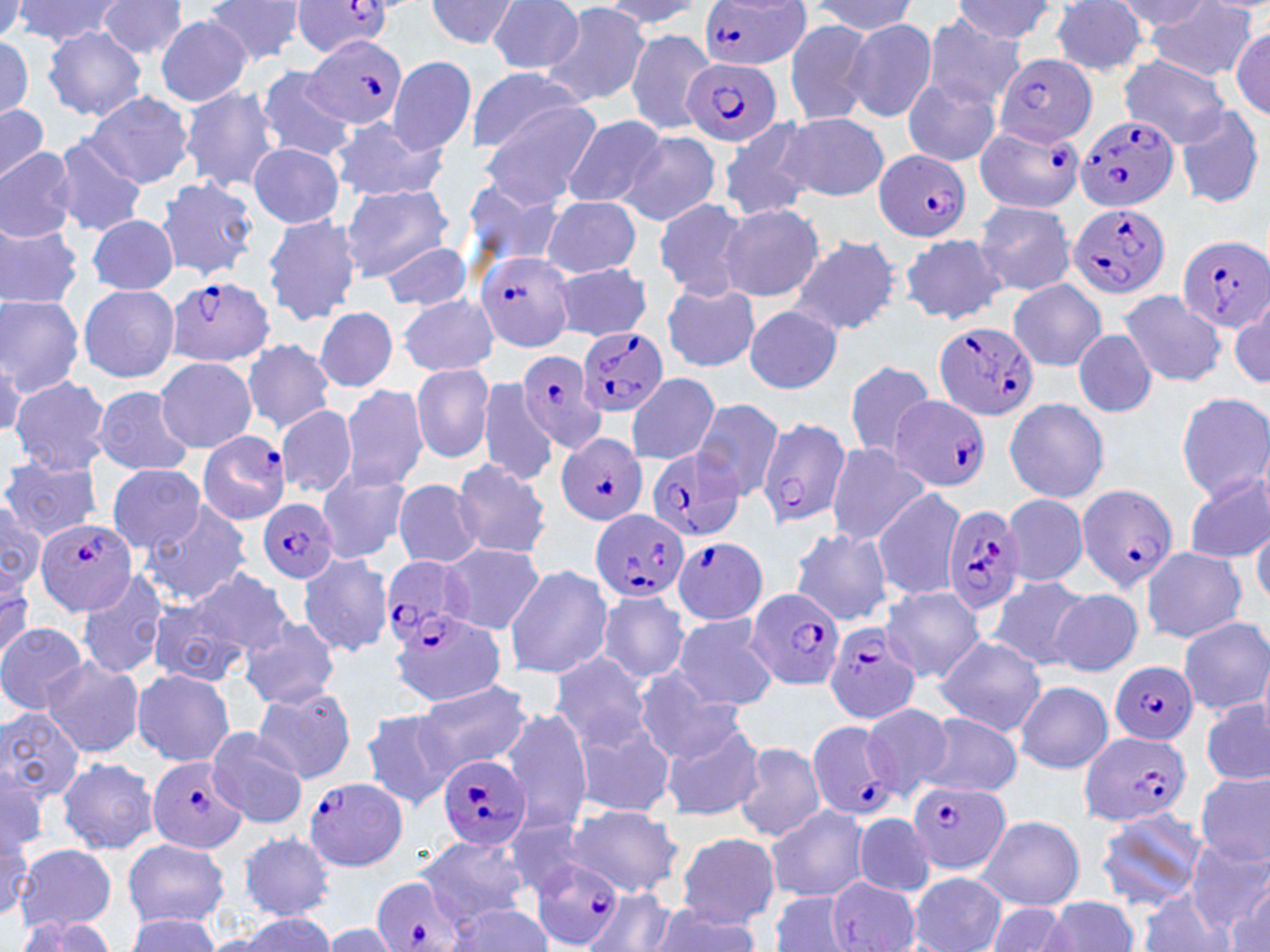
Summary:
  - Coordinate format: approximate bounding boxes as (x1, y1, x2, y2) in pixels
  - Uninfected red blood cell locations: (0, 0, 28, 38), (14, 0, 125, 47), (200, 0, 308, 65), (424, 0, 520, 51), (594, 0, 705, 29), (96, 1, 188, 60), (808, 1, 918, 35), (953, 1, 1058, 45), (1114, 1, 1216, 30), (486, 2, 585, 74), (538, 2, 653, 109), (1049, 2, 1152, 78), (1145, 2, 1257, 82), (155, 14, 255, 106), (781, 17, 879, 127), (923, 17, 1023, 111), (844, 19, 938, 122), (42, 25, 148, 121), (626, 27, 717, 135), (1231, 27, 1268, 118), (0, 31, 38, 121), (386, 56, 477, 156), (1118, 56, 1232, 147), (255, 65, 356, 162), (465, 68, 591, 154), (902, 77, 1001, 169), (178, 86, 282, 194), (84, 90, 195, 189), (478, 98, 605, 204), (0, 102, 52, 186), (1174, 105, 1266, 210), (779, 113, 888, 202), (564, 115, 668, 209), (717, 116, 817, 221), (328, 117, 447, 204), (548, 124, 656, 270), (619, 130, 722, 227), (51, 136, 149, 237), (247, 141, 345, 228), (0, 145, 77, 243), (456, 174, 567, 273), (155, 178, 259, 281), (339, 182, 457, 281), (541, 196, 642, 277), (653, 196, 750, 299), (974, 200, 1076, 296), (719, 203, 825, 301), (261, 212, 360, 328), (86, 214, 179, 295), (739, 214, 883, 320), (0, 221, 84, 310), (899, 231, 1008, 325), (788, 234, 900, 337), (376, 240, 473, 310), (550, 263, 652, 341), (1007, 279, 1107, 372), (661, 282, 760, 373), (78, 283, 181, 385), (1118, 290, 1227, 388), (0, 293, 86, 395), (398, 293, 498, 378), (1231, 294, 1269, 385), (742, 306, 845, 392), (312, 307, 399, 392), (1070, 329, 1159, 418), (244, 339, 337, 432), (0, 341, 27, 441), (155, 358, 258, 452), (843, 360, 938, 460), (411, 363, 496, 465), (625, 373, 721, 465), (9, 375, 111, 477), (477, 378, 560, 490), (339, 382, 429, 491), (91, 386, 195, 476), (1175, 391, 1270, 501), (1002, 398, 1111, 503), (692, 399, 787, 501), (276, 404, 358, 498), (825, 443, 930, 547), (2, 456, 104, 540), (451, 458, 550, 559), (105, 464, 206, 553), (314, 468, 415, 564), (1183, 471, 1269, 565), (393, 479, 482, 568), (871, 489, 968, 599), (1001, 492, 1089, 586), (139, 498, 254, 606), (0, 502, 47, 593), (1252, 514, 1269, 607), (789, 527, 894, 627), (440, 544, 543, 634), (1140, 546, 1246, 643), (296, 552, 394, 658), (0, 562, 38, 661), (504, 564, 612, 679), (187, 566, 295, 660), (74, 570, 171, 680), (986, 575, 1089, 671), (880, 586, 986, 682), (597, 588, 692, 685), (1050, 589, 1143, 677), (146, 597, 252, 688), (670, 614, 775, 711), (239, 615, 341, 708), (1178, 616, 1270, 715), (0, 622, 90, 714), (934, 636, 1047, 736), (548, 653, 655, 755), (41, 656, 145, 759), (133, 668, 236, 768), (630, 669, 743, 763), (411, 681, 531, 775), (1015, 681, 1113, 773), (252, 685, 357, 785), (1202, 698, 1269, 787), (859, 701, 953, 800), (498, 705, 595, 833), (0, 706, 85, 800), (358, 709, 455, 810), (569, 712, 677, 819), (918, 712, 1021, 797), (659, 716, 765, 822), (205, 727, 311, 830), (732, 742, 825, 843), (57, 757, 160, 855), (0, 765, 48, 859), (1193, 771, 1270, 865), (564, 804, 682, 896), (765, 805, 868, 901), (1096, 808, 1207, 910), (854, 813, 935, 898), (976, 815, 1086, 911), (500, 816, 592, 898), (238, 832, 335, 921), (675, 832, 778, 928), (417, 834, 527, 925), (1185, 836, 1270, 933), (122, 837, 230, 928), (17, 843, 117, 932), (908, 871, 1005, 952), (826, 875, 921, 952), (1230, 878, 1270, 951), (583, 887, 676, 952), (1137, 887, 1234, 952), (770, 891, 855, 951), (1040, 896, 1142, 952), (448, 902, 553, 951), (649, 905, 762, 952), (981, 905, 1077, 952), (122, 913, 225, 950), (221, 913, 340, 951), (10, 916, 120, 951), (321, 923, 402, 951)
  - Plasmodium falciparum-infected red blood cell locations: (290, 1, 396, 56), (697, 1, 813, 72), (305, 33, 409, 132), (993, 52, 1098, 146), (682, 57, 780, 149), (1075, 113, 1180, 213), (973, 122, 1083, 216), (872, 149, 974, 242), (1067, 204, 1172, 298), (1176, 236, 1270, 331), (476, 250, 575, 353), (163, 276, 275, 367), (933, 320, 1039, 423), (574, 327, 667, 417), (515, 350, 611, 453), (890, 396, 989, 492), (757, 415, 851, 528), (199, 429, 290, 524), (555, 432, 649, 527), (645, 446, 745, 542), (1074, 483, 1178, 589), (259, 497, 340, 585), (942, 503, 1026, 615), (591, 510, 690, 603), (38, 515, 138, 617), (672, 536, 769, 626), (376, 554, 474, 647), (748, 589, 846, 691), (824, 621, 922, 724), (1109, 661, 1197, 744), (804, 719, 900, 822), (1079, 731, 1193, 827), (438, 754, 532, 849), (148, 757, 249, 853), (304, 777, 409, 871), (909, 782, 1010, 874), (529, 857, 625, 949), (371, 877, 466, 952)
  - Slide-level diagnosis: Plasmodium falciparum
  - Image size: 1270×952 pixels
  - Modality: optical microscopy
  - Magnification: 1000x
  - Preparation: thin blood smear
  - Field of view: one of a larger specimen
  - Stain: May-Grünwald-Giemsa